Assess this cell for malaria.
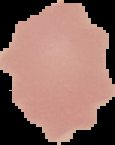
Uninfected.

From a thin blood film. Image is 115×145 pixels. The area outside the segmented cell region is set to black.